Describe the morphology of the erythrocytes.
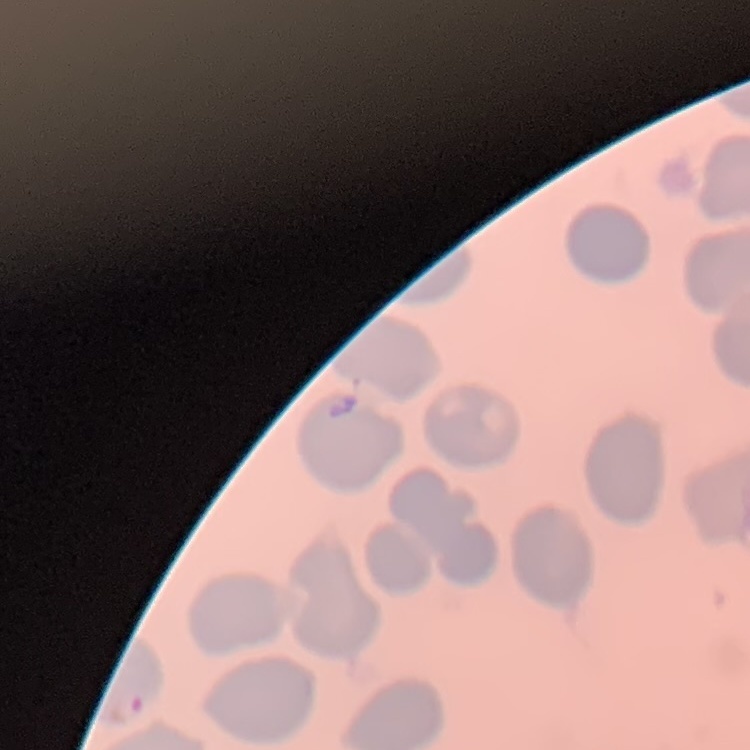

They show no rouleaux formation.

Summary:
  - Preparation: thin blood smear
  - Image type: one tile cut from a larger photomicrograph
  - Stain: Field's or Giemsa